Give the extent of all uninfected red blood cells.
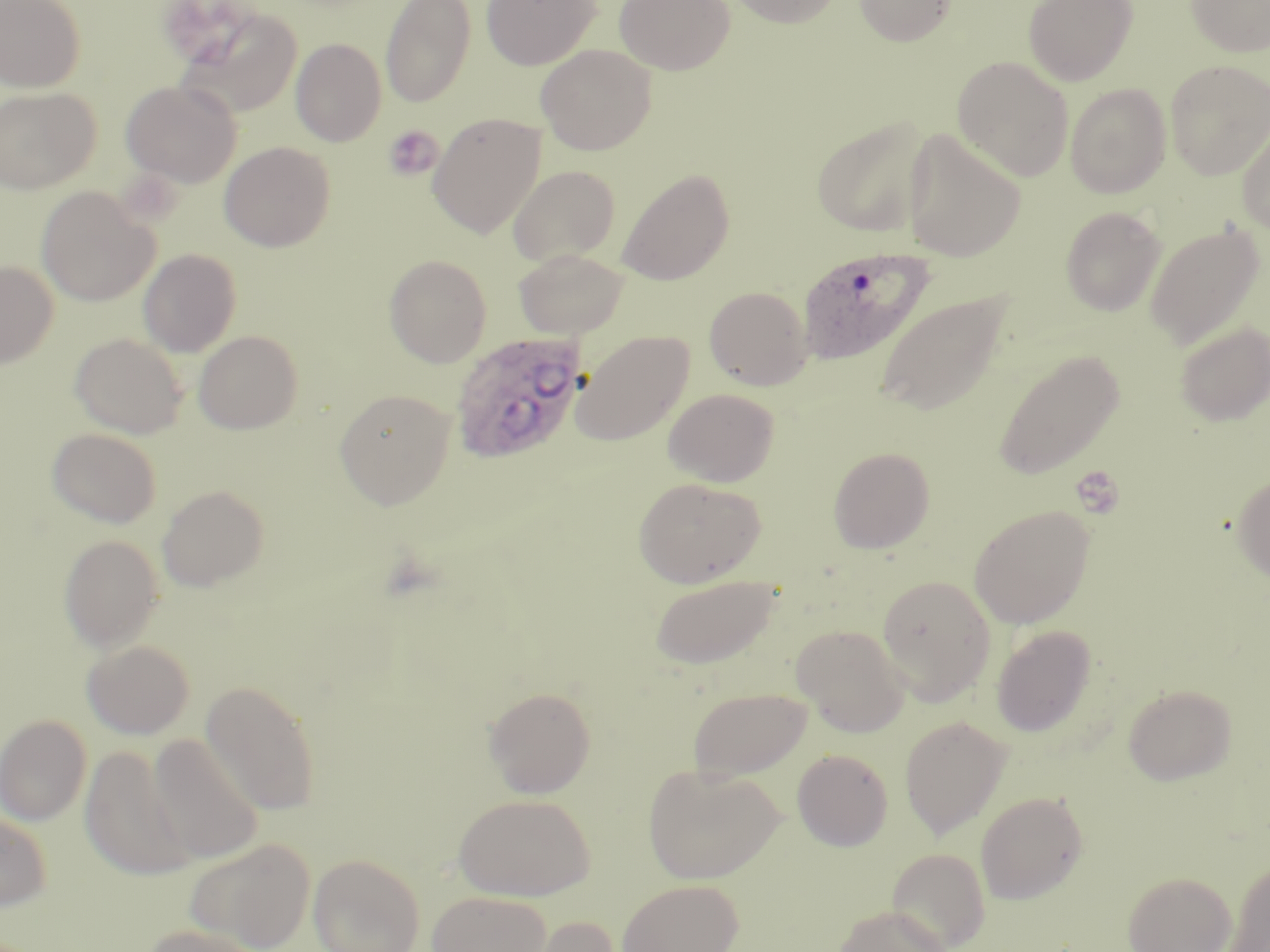
Approximate bounding boxes as [x1, y1, x2, y2] in pixels.
Uninfected red blood cells: [0, 0, 85, 92], [380, 0, 475, 108], [481, 0, 601, 70], [614, 0, 735, 75], [726, 0, 842, 28], [854, 0, 957, 47], [1023, 0, 1138, 86], [1185, 0, 1270, 57], [176, 5, 303, 118], [291, 38, 386, 146], [535, 44, 656, 154], [952, 56, 1074, 182], [1165, 60, 1270, 180], [121, 79, 241, 188], [1065, 83, 1171, 198], [0, 87, 100, 193], [428, 113, 545, 238], [811, 116, 933, 238], [1236, 119, 1270, 236], [899, 129, 1026, 263], [220, 142, 335, 252], [508, 165, 621, 267], [616, 168, 735, 286], [36, 186, 158, 307], [1060, 206, 1167, 316], [1145, 222, 1266, 351], [139, 249, 241, 357], [514, 249, 629, 339], [384, 254, 492, 367], [0, 260, 58, 369], [704, 285, 812, 390], [874, 288, 1013, 417], [1173, 320, 1270, 426], [194, 330, 303, 434], [571, 330, 694, 445], [69, 332, 188, 438], [992, 349, 1124, 481], [663, 387, 780, 487], [335, 388, 456, 510], [47, 427, 162, 528], [828, 447, 935, 554], [1232, 471, 1270, 583], [633, 477, 766, 588], [157, 484, 269, 591], [969, 506, 1094, 628], [58, 534, 165, 651], [648, 574, 782, 669], [876, 574, 996, 705], [793, 624, 909, 736], [991, 625, 1096, 737], [82, 640, 195, 739], [201, 680, 321, 816], [1122, 683, 1237, 786], [483, 686, 597, 798], [687, 686, 813, 780], [0, 714, 91, 826], [899, 716, 1012, 840], [147, 733, 264, 864], [80, 745, 195, 880], [792, 748, 894, 851], [642, 763, 784, 884], [975, 791, 1089, 904], [453, 793, 595, 902], [0, 809, 52, 911], [184, 838, 315, 951], [887, 848, 991, 951], [308, 853, 425, 952], [1224, 858, 1270, 952], [1123, 870, 1236, 952], [616, 879, 743, 952], [427, 891, 552, 952], [832, 904, 952, 952], [522, 915, 621, 952], [138, 923, 263, 952].

Summary:
  - Plasmodium ovale-infected red blood cell locations: [797, 246, 935, 366], [450, 331, 589, 464]
  - Platelet locations: [383, 125, 443, 181], [1071, 467, 1125, 520]
  - Slide-level diagnosis: Plasmodium ovale
  - Stain: May-Grünwald-Giemsa
  - Magnification: 1000x
  - Field of view: one of a larger specimen
  - Modality: light microscopy
  - Image size: 1270×952 pixels
  - Preparation: thin blood smear